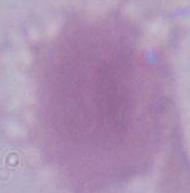

Captured at 1000x magnification. Micrograph. An erythrocyte is shown.